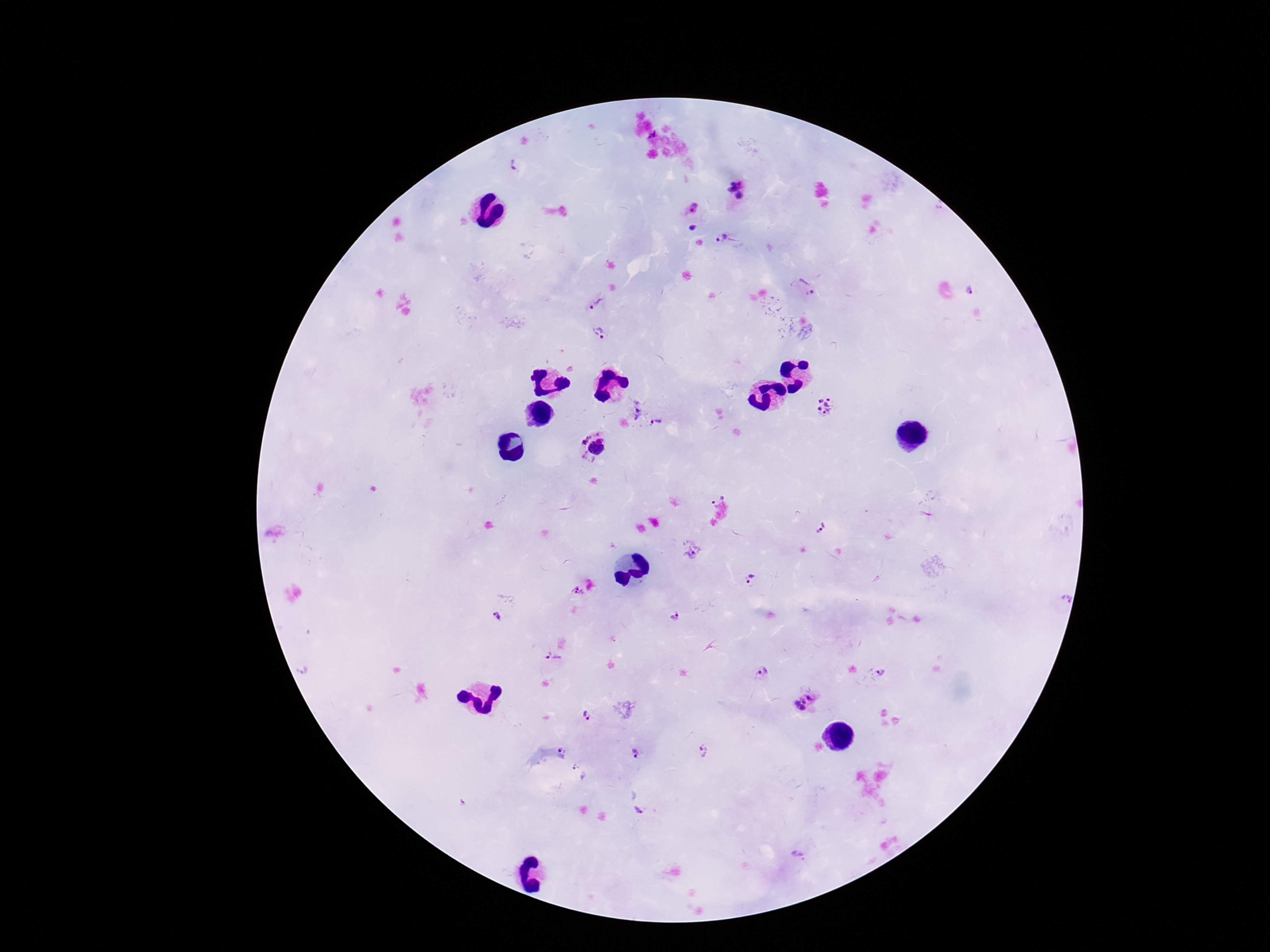

Approximate object centers, in pixels from the top-left corner. Plasmodium parasite locations: (x=513, y=166), (x=735, y=190), (x=693, y=207), (x=691, y=227), (x=724, y=239), (x=806, y=285), (x=970, y=288), (x=596, y=302), (x=598, y=333), (x=826, y=407), (x=633, y=411), (x=656, y=424), (x=582, y=437), (x=600, y=437), (x=584, y=456), (x=712, y=502), (x=819, y=526), (x=690, y=550), (x=751, y=580), (x=577, y=592), (x=675, y=616), (x=498, y=617), (x=553, y=661), (x=304, y=670), (x=763, y=671), (x=882, y=673), (x=805, y=703), (x=586, y=716), (x=562, y=750), (x=702, y=751), (x=635, y=752), (x=579, y=772), (x=638, y=812), (x=798, y=854). Giemsa-stained preparation. 100x magnification. Image is 1270×952 pixels. Thick blood smear. Patient malaria status: infected. Photographed through the microscope eyepiece with a smartphone camera. One field from this slide.